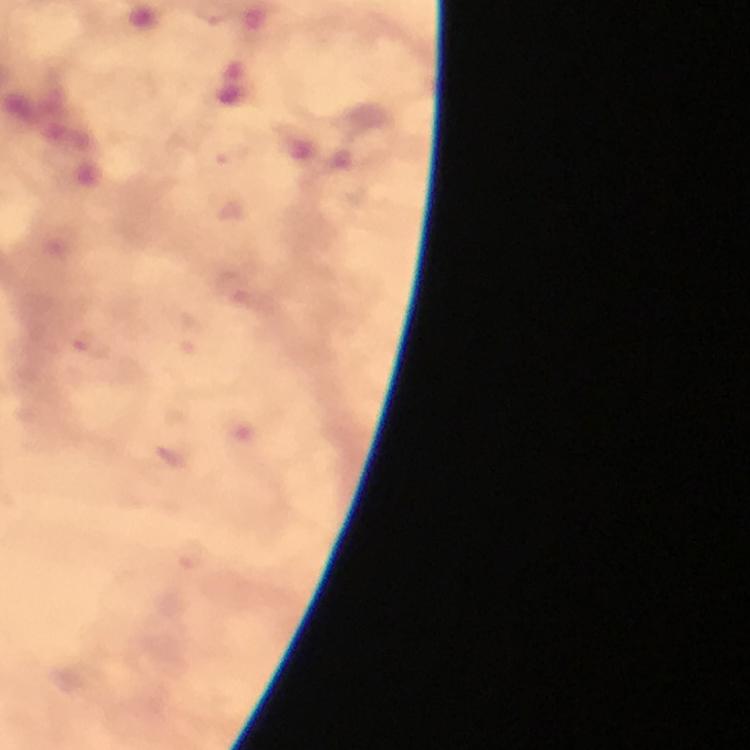

cropped from = one field of view
preparation = thick blood smear
capture = smartphone photograph through a microscope
stain = Giemsa
context = from a malaria diagnostic workup
magnification = 100x
image size = 750×750 pixels
malaria parasite locations = approximate centers as (x, y) in pixels: (234, 287), (82, 341), (191, 554)
immersion oil = used